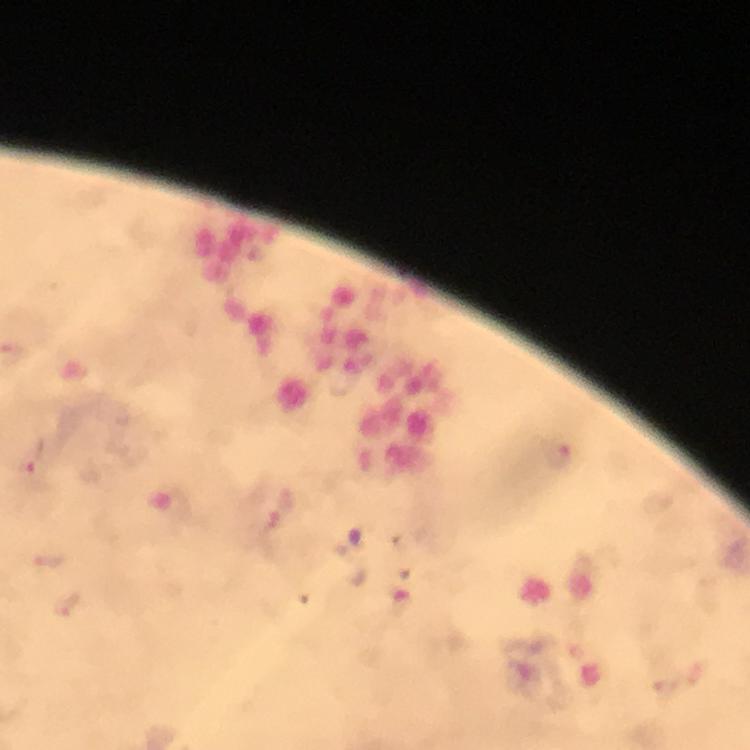

Approximate centers as [x, y] in pixels. Plasmodium parasite locations: [561, 453], [34, 457], [282, 511]. A crop from one field of view. Thick blood film. Photographed through the microscope with a smartphone camera. From a malaria diagnostic workup. Image is 750×750 pixels. Immersion oil applied. 100x magnification. Giemsa stain.